Report the malaria status of this cell.
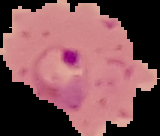

Parasitized.

Summary:
  - Preparation: thin blood film
  - Image type: segmented cell region on a black background
  - Image size: 160×136 pixels